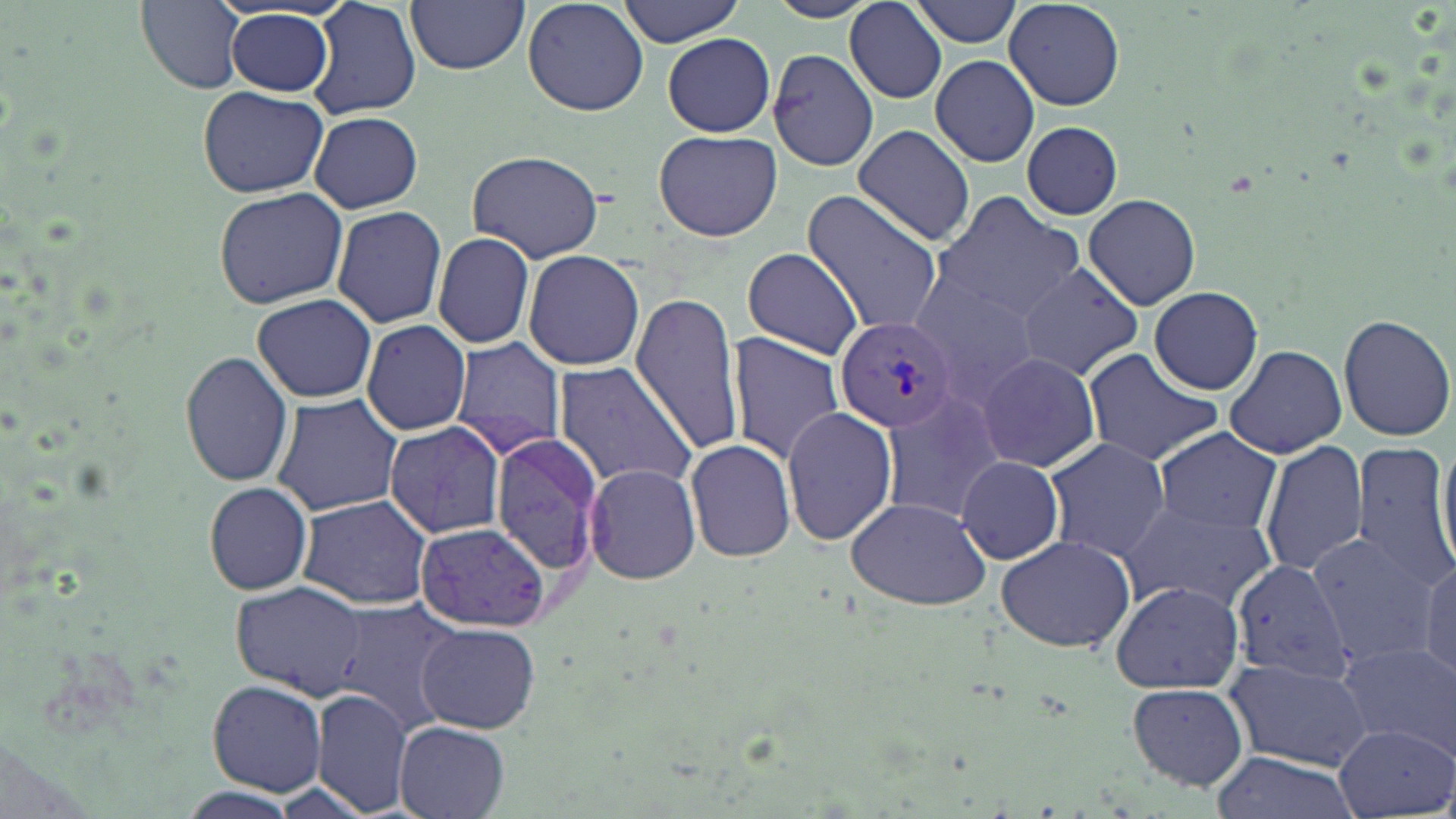

Summary:
  - Coordinate format: approximate bounding boxes as (x1,y1)-(x2,y2) corner pairs in pixels
  - Plasmodium vivax-infected red blood cell locations: (835,317)-(958,431)
  - Uninfected red blood cell locations: (137,0)-(247,91), (307,0)-(423,120), (521,0)-(650,118), (618,0)-(746,46), (909,0)-(1024,47), (405,1)-(530,74), (1005,1)-(1126,109), (846,4)-(947,104), (224,9)-(335,98), (662,33)-(775,137), (768,45)-(880,171), (930,54)-(1040,167), (198,86)-(327,199), (309,110)-(423,212), (1020,120)-(1123,219), (853,124)-(976,248), (653,130)-(782,241), (466,147)-(606,264), (213,186)-(349,309), (800,189)-(943,336), (929,191)-(1084,323), (1083,192)-(1202,311), (331,204)-(448,328), (432,231)-(537,351), (739,247)-(867,359), (523,250)-(646,371), (1014,261)-(1144,382), (908,281)-(1042,402), (1148,285)-(1263,395), (628,292)-(746,456), (252,293)-(377,403), (1336,313)-(1455,441), (361,319)-(472,436), (727,332)-(847,464), (452,336)-(568,460), (1224,343)-(1349,460), (1083,348)-(1225,466), (975,351)-(1102,473), (181,353)-(294,487), (553,362)-(701,491), (880,390)-(1004,525), (271,393)-(404,516), (782,406)-(900,546), (383,421)-(506,538), (1153,428)-(1282,535), (491,431)-(605,580), (1434,435)-(1455,572), (683,438)-(797,563), (1042,438)-(1171,564), (1260,439)-(1369,579), (1350,441)-(1455,592), (956,455)-(1064,565), (585,461)-(701,584), (204,482)-(313,596), (295,495)-(432,609), (843,496)-(993,610), (1117,499)-(1277,616), (416,522)-(551,632), (1305,532)-(1436,665), (994,534)-(1137,654), (1418,554)-(1456,685), (1227,555)-(1356,722), (1108,579)-(1245,695), (231,581)-(368,698), (330,598)-(460,731), (415,621)-(541,733), (1336,641)-(1455,749), (1224,657)-(1371,769), (208,681)-(327,796), (1126,682)-(1250,791), (313,687)-(414,817), (394,721)-(511,818), (1336,722)-(1455,818), (1210,751)-(1358,819)
  - Slide-level diagnosis: Plasmodium vivax
  - Modality: light microscopy
  - Stain: May-Grünwald-Giemsa
  - Preparation: thin blood smear
  - Field of view: single
  - Image size: 1456×819 pixels
  - Magnification: 1000x